Locate every blood parasite and identify its species.
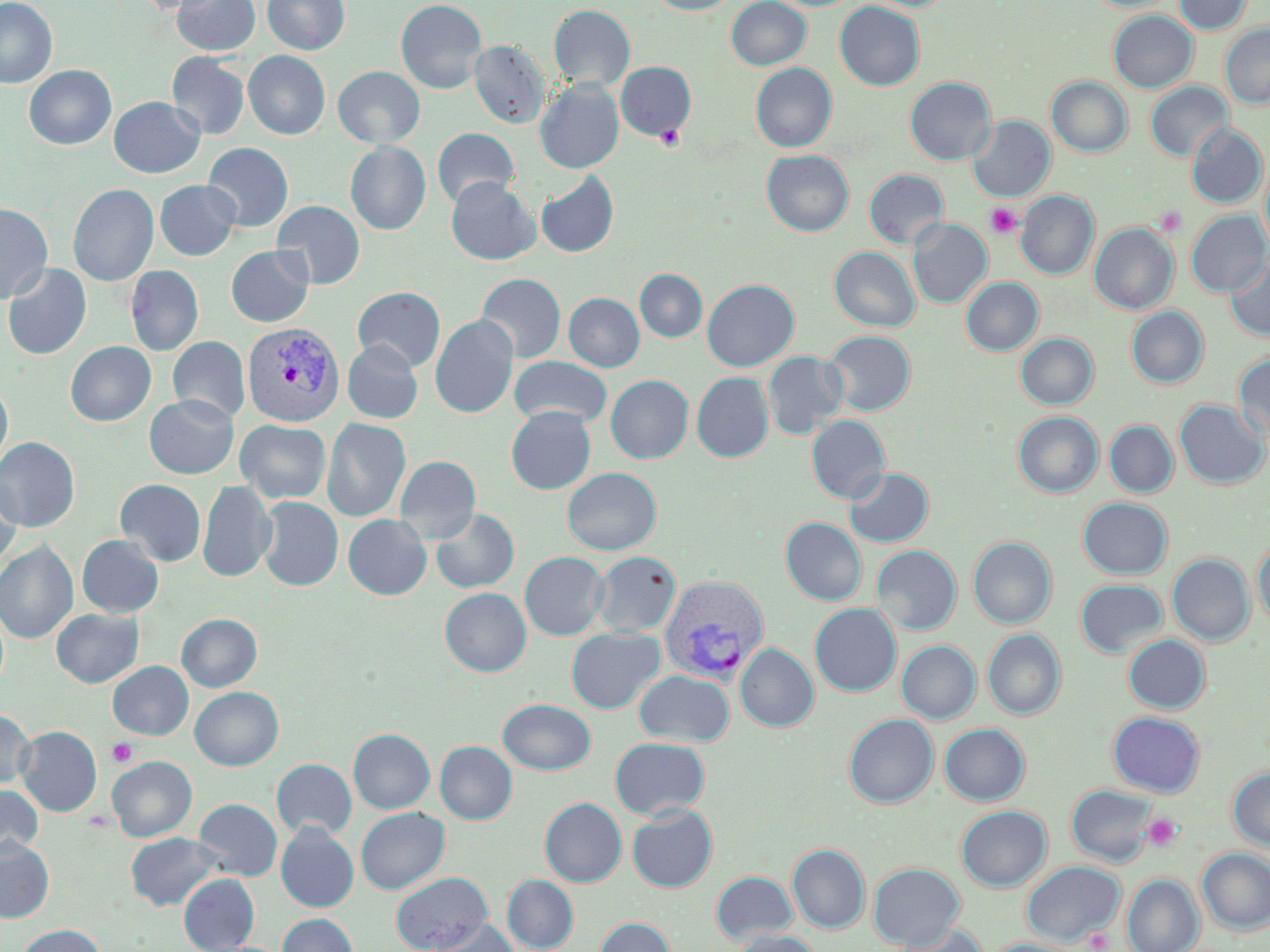
Approximate bounding boxes as named x1/y1/x2/y2 corners in pixels.
Plasmodium vivax-infected red blood cells: (x1=243, y1=321, x2=345, y2=427), (x1=659, y1=575, x2=769, y2=682).
No Plasmodium falciparum, Plasmodium ovale, Plasmodium malariae, Babesia divergens, or Trypanosoma brucei observed.

Uninfected red blood cell locations: (x1=0, y1=0, x2=57, y2=88), (x1=133, y1=0, x2=225, y2=14), (x1=172, y1=0, x2=260, y2=55), (x1=263, y1=0, x2=349, y2=54), (x1=395, y1=0, x2=487, y2=94), (x1=645, y1=0, x2=739, y2=14), (x1=726, y1=0, x2=811, y2=70), (x1=1085, y1=0, x2=1177, y2=13), (x1=1174, y1=0, x2=1252, y2=34), (x1=835, y1=1, x2=924, y2=91), (x1=548, y1=4, x2=635, y2=91), (x1=1108, y1=10, x2=1197, y2=92), (x1=1220, y1=24, x2=1270, y2=108), (x1=469, y1=40, x2=550, y2=128), (x1=243, y1=50, x2=330, y2=139), (x1=167, y1=52, x2=249, y2=139), (x1=616, y1=61, x2=696, y2=141), (x1=750, y1=63, x2=837, y2=152), (x1=24, y1=65, x2=116, y2=150), (x1=333, y1=66, x2=425, y2=148), (x1=904, y1=76, x2=996, y2=165), (x1=1047, y1=77, x2=1132, y2=156), (x1=535, y1=78, x2=624, y2=174), (x1=1145, y1=81, x2=1232, y2=161), (x1=109, y1=96, x2=204, y2=178), (x1=967, y1=116, x2=1055, y2=202), (x1=1187, y1=123, x2=1267, y2=209), (x1=432, y1=128, x2=519, y2=208), (x1=345, y1=140, x2=431, y2=235), (x1=203, y1=142, x2=293, y2=231), (x1=761, y1=150, x2=854, y2=236), (x1=1260, y1=158, x2=1270, y2=255), (x1=864, y1=169, x2=948, y2=248), (x1=535, y1=171, x2=619, y2=258), (x1=446, y1=177, x2=540, y2=265), (x1=155, y1=180, x2=240, y2=260), (x1=68, y1=183, x2=159, y2=286), (x1=1016, y1=191, x2=1099, y2=279), (x1=272, y1=200, x2=365, y2=289), (x1=0, y1=203, x2=52, y2=303), (x1=1186, y1=210, x2=1269, y2=296), (x1=908, y1=219, x2=991, y2=308), (x1=1090, y1=223, x2=1178, y2=314), (x1=226, y1=246, x2=313, y2=327), (x1=829, y1=246, x2=919, y2=331), (x1=1225, y1=251, x2=1270, y2=341), (x1=2, y1=262, x2=91, y2=360), (x1=125, y1=265, x2=203, y2=356), (x1=635, y1=269, x2=707, y2=342), (x1=476, y1=273, x2=566, y2=363), (x1=961, y1=277, x2=1043, y2=355), (x1=702, y1=279, x2=799, y2=371), (x1=353, y1=286, x2=445, y2=372), (x1=563, y1=293, x2=644, y2=372), (x1=1126, y1=306, x2=1208, y2=388), (x1=431, y1=315, x2=519, y2=418), (x1=823, y1=330, x2=915, y2=415), (x1=1016, y1=333, x2=1098, y2=409), (x1=168, y1=336, x2=250, y2=423), (x1=65, y1=341, x2=155, y2=426), (x1=342, y1=341, x2=423, y2=423), (x1=763, y1=351, x2=848, y2=439), (x1=1233, y1=352, x2=1270, y2=444), (x1=509, y1=356, x2=612, y2=428), (x1=691, y1=372, x2=773, y2=462), (x1=605, y1=374, x2=692, y2=463), (x1=0, y1=380, x2=13, y2=471), (x1=144, y1=394, x2=238, y2=478), (x1=1174, y1=399, x2=1269, y2=489), (x1=506, y1=406, x2=596, y2=494), (x1=1013, y1=411, x2=1103, y2=497), (x1=806, y1=415, x2=890, y2=503), (x1=322, y1=418, x2=410, y2=522), (x1=235, y1=420, x2=331, y2=503), (x1=1104, y1=421, x2=1178, y2=498), (x1=0, y1=437, x2=80, y2=531), (x1=395, y1=455, x2=481, y2=542), (x1=844, y1=466, x2=933, y2=547), (x1=562, y1=467, x2=661, y2=555), (x1=0, y1=477, x2=22, y2=569), (x1=115, y1=479, x2=206, y2=565), (x1=198, y1=481, x2=276, y2=581), (x1=256, y1=496, x2=343, y2=591), (x1=1078, y1=497, x2=1172, y2=578), (x1=430, y1=508, x2=519, y2=593), (x1=343, y1=514, x2=431, y2=599), (x1=780, y1=517, x2=866, y2=606), (x1=77, y1=535, x2=164, y2=618), (x1=968, y1=536, x2=1056, y2=628), (x1=1253, y1=537, x2=1270, y2=630), (x1=0, y1=541, x2=78, y2=643), (x1=872, y1=545, x2=961, y2=634), (x1=520, y1=551, x2=608, y2=640), (x1=591, y1=551, x2=680, y2=636), (x1=1168, y1=554, x2=1255, y2=645), (x1=1075, y1=579, x2=1167, y2=658), (x1=440, y1=588, x2=531, y2=676), (x1=810, y1=602, x2=901, y2=696), (x1=51, y1=608, x2=144, y2=687), (x1=177, y1=613, x2=262, y2=691), (x1=565, y1=627, x2=664, y2=713), (x1=983, y1=629, x2=1066, y2=720), (x1=1123, y1=634, x2=1210, y2=714), (x1=897, y1=640, x2=980, y2=723), (x1=735, y1=643, x2=818, y2=731), (x1=107, y1=661, x2=193, y2=739), (x1=634, y1=669, x2=734, y2=746), (x1=190, y1=686, x2=283, y2=770), (x1=498, y1=699, x2=595, y2=774), (x1=0, y1=709, x2=34, y2=789), (x1=1107, y1=711, x2=1205, y2=797), (x1=844, y1=713, x2=938, y2=807), (x1=939, y1=723, x2=1030, y2=805), (x1=16, y1=726, x2=101, y2=816), (x1=348, y1=728, x2=434, y2=813), (x1=610, y1=737, x2=710, y2=820), (x1=435, y1=741, x2=517, y2=824), (x1=107, y1=755, x2=196, y2=841), (x1=272, y1=758, x2=356, y2=839), (x1=1228, y1=767, x2=1270, y2=852), (x1=0, y1=784, x2=42, y2=859), (x1=1067, y1=784, x2=1156, y2=866), (x1=193, y1=798, x2=282, y2=880), (x1=539, y1=798, x2=626, y2=886), (x1=627, y1=805, x2=717, y2=892), (x1=956, y1=805, x2=1051, y2=891), (x1=355, y1=807, x2=449, y2=893), (x1=275, y1=822, x2=358, y2=912), (x1=125, y1=832, x2=220, y2=911), (x1=0, y1=839, x2=54, y2=922), (x1=788, y1=844, x2=869, y2=933), (x1=1197, y1=848, x2=1270, y2=935), (x1=1022, y1=861, x2=1124, y2=946), (x1=868, y1=862, x2=965, y2=950), (x1=390, y1=871, x2=492, y2=952), (x1=711, y1=871, x2=798, y2=943), (x1=178, y1=873, x2=258, y2=952), (x1=502, y1=874, x2=578, y2=952), (x1=1123, y1=875, x2=1204, y2=952), (x1=278, y1=913, x2=357, y2=952), (x1=594, y1=917, x2=676, y2=952), (x1=426, y1=919, x2=517, y2=952), (x1=890, y1=923, x2=987, y2=952), (x1=16, y1=924, x2=105, y2=952), (x1=729, y1=930, x2=822, y2=952), (x1=983, y1=939, x2=1079, y2=952). Platelet locations: (x1=655, y1=124, x2=685, y2=151), (x1=986, y1=203, x2=1022, y2=238), (x1=1153, y1=206, x2=1185, y2=236), (x1=107, y1=738, x2=138, y2=767), (x1=1142, y1=813, x2=1182, y2=852), (x1=1085, y1=928, x2=1113, y2=951). Slide-level diagnosis: Plasmodium vivax. Captured at 1000x magnification. Image is 1270×952 pixels. Optical microscopy. Thin blood smear. Single field of view. May-Grünwald-Giemsa stain.